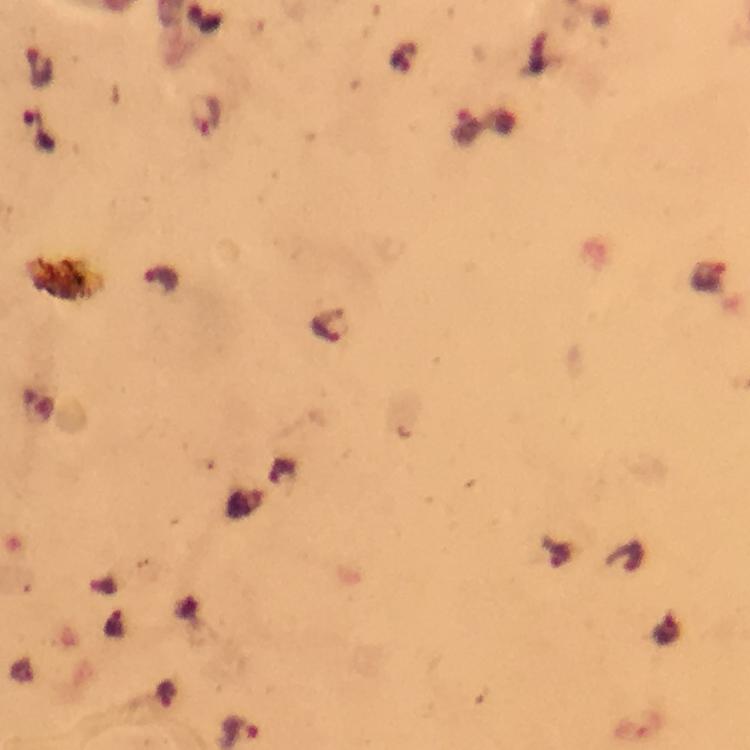
Approximate object centers, in pixels from the top-left corner. Plasmodium parasite locations: (x=39, y=67), (x=207, y=116), (x=467, y=127), (x=162, y=281), (x=330, y=325). Giemsa stain. Cropped region of a single field of view. Image is 750×750 pixels. Immersion oil applied. Smartphone photograph taken through a microscope. From a malaria diagnostic workup. Thick blood smear. 100x magnification.